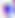
Summary:
  - Identification: Toxoplasma gondii
  - Magnification: 400x
  - Modality: photomicrograph